Describe the morphology of the erythrocytes.
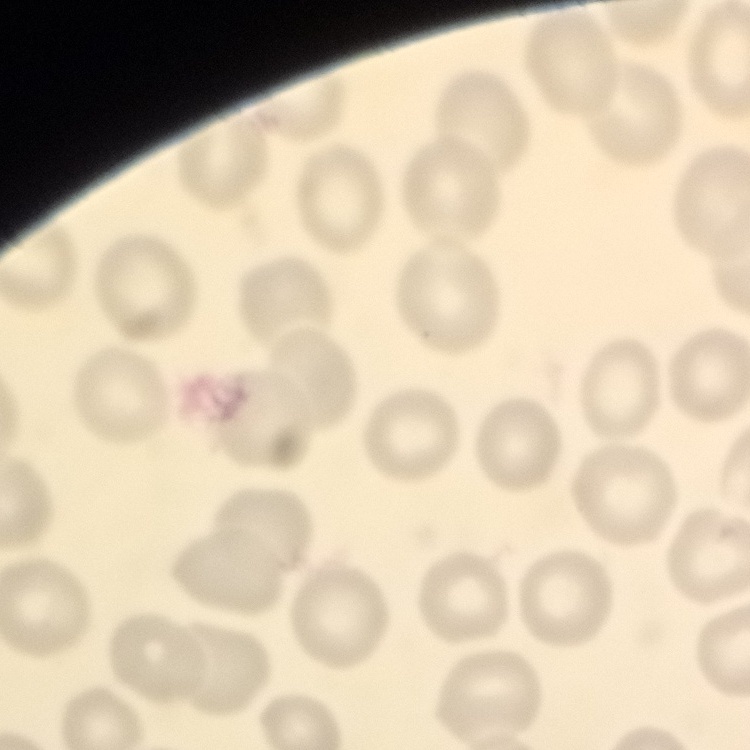

They show no rouleaux formation.

Summary:
  - Stain: Field's or Giemsa
  - Image type: square crop of a larger photomicrograph
  - Preparation: thin peripheral smear